Name the cell type shown.
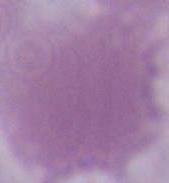
An erythrocyte.

modality: photomicrograph
magnification: 1000x